Locate every malaria parasite and every leukocyte.
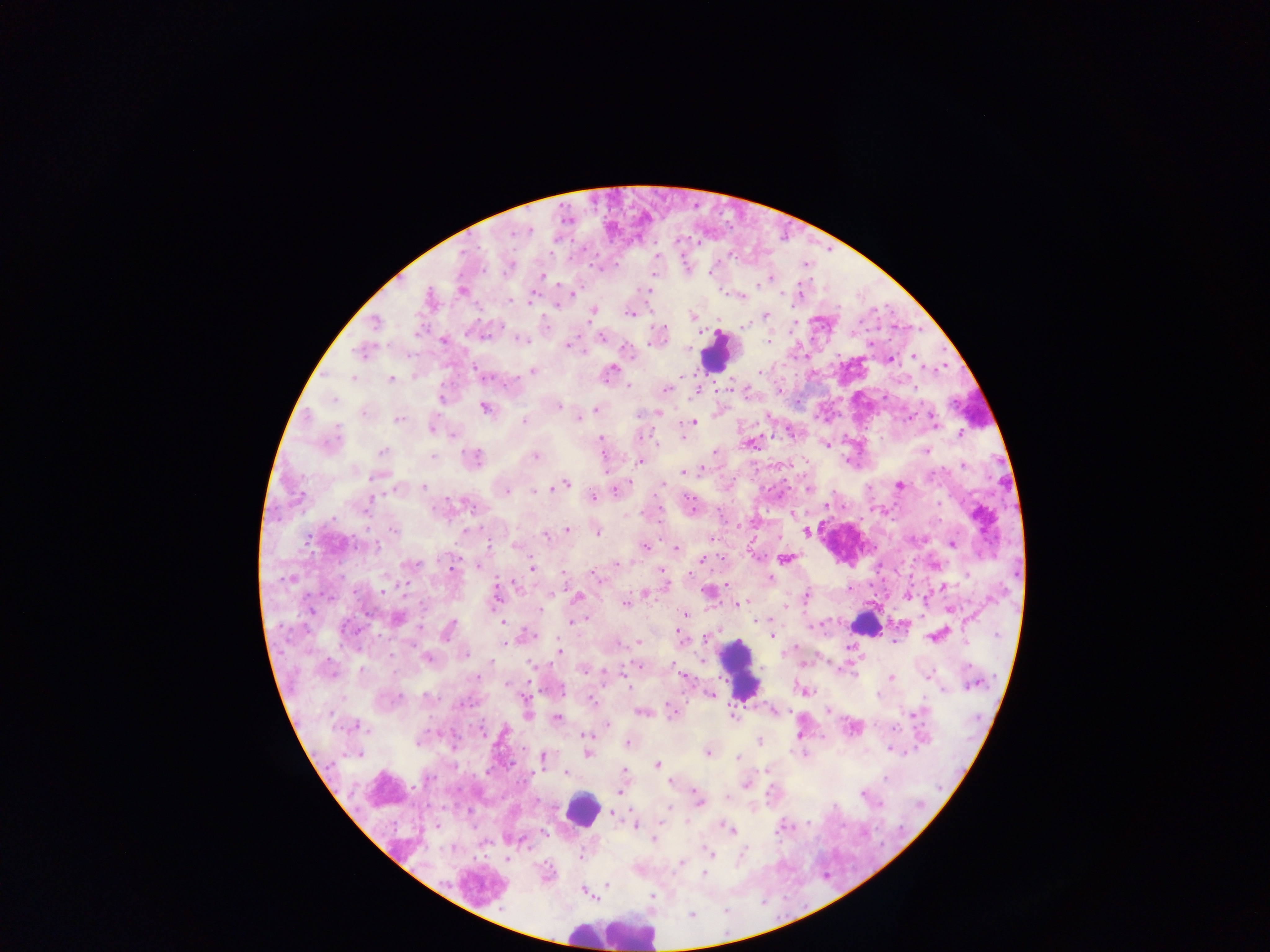

Approximate centers as x y in pixels.
Malaria parasites: 656 257; 509 268; 711 271; 541 276; 761 282; 461 290; 646 290; 574 294; 741 296; 429 298; 530 301; 556 303; 592 312; 629 313; 765 315; 693 317; 375 323; 744 326; 602 336; 444 339; 520 339; 567 345; 362 352; 913 356; 889 360; 478 371; 533 371; 610 371; 414 376; 352 378; 391 379; 629 385; 666 390; 696 391; 780 391; 442 398; 333 400; 557 406; 484 408; 596 409; 656 412; 640 415; 579 417; 398 419; 525 421; 693 423; 934 423; 432 426; 960 434; 454 435; 599 440; 750 443; 826 444; 714 451; 926 451; 382 452; 431 456; 535 456; 473 458; 639 461; 789 464; 963 466; 703 467; 684 471; 378 475; 566 484; 898 485; 423 487; 551 487; 617 489; 808 489; 505 490; 592 497; 368 501; 464 501; 827 506; 691 507; 792 513; 395 529; 567 529; 465 531; 807 531; 597 532; 545 534; 951 543; 516 545; 644 546; 676 549; 785 558; 703 559; 934 564; 478 565; 616 565; 409 566; 453 569; 532 569; 662 571; 594 574; 288 578; 769 579; 726 584; 516 586; 942 587; 644 592; 708 592; 907 595; 496 596; 577 597; 806 597; 625 603; 735 605; 784 606; 949 609; 685 614; 396 619; 757 620; 574 621; 503 622; 449 631; 679 634; 528 635; 937 635; 772 636; 638 641; 504 644; 559 652; 464 653; 427 658; 702 661; 491 663; 529 664; 638 665; 583 670; 361 671; 927 676; 683 677; 890 677; 478 678; 624 678; 507 684; 804 691; 709 694; 590 699; 527 700; 774 709; 828 710; 641 711; 669 711; 526 713; 916 715; 733 716; 556 719; 606 724; 355 726; 852 727; 480 730; 584 735; 760 741; 628 742; 455 747; 890 750; 587 753; 708 753; 541 758; 739 758; 657 764; 766 770; 488 771; 565 771; 623 771; 671 782; 745 783; 619 792; 863 793; 726 796; 698 799; 613 811; 634 825; 731 828; 544 833; 654 838; 707 852; 506 859; 681 862; 703 873; 607 885; 584 890.
Leukocytes: 716 352; 865 623; 739 669; 582 810; 614 932.

Summary:
  - Capture: mobile-phone photograph through a microscope
  - Field of view: single
  - Country: Ghana
  - Preparation: thick blood smear
  - Image size: 1270×952 pixels